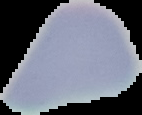
Summary:
  - Result: no Plasmodium parasites seen
  - Preparation: thin blood smear
  - Image type: cell region segmented out of the field of view; surrounding area masked to black
  - Image size: 142×115 pixels